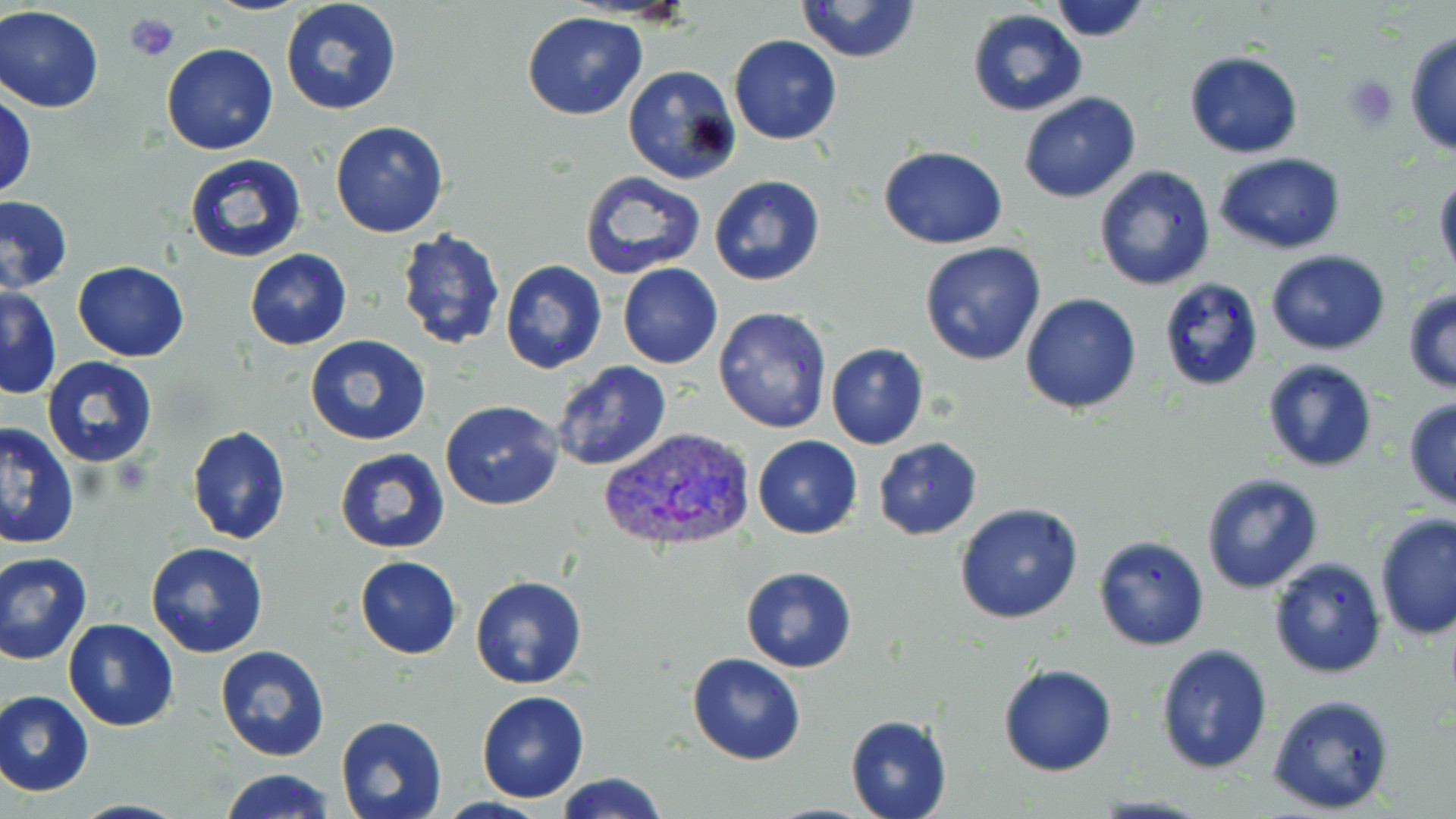
slide-level diagnosis = Plasmodium vivax
modality = light microscopy
magnification = 1000x
platelet locations = approximate bounding boxes as named x1/y1/x2/y2 corners in pixels: (x1=124, y1=11, x2=179, y2=65), (x1=1343, y1=76, x2=1398, y2=130)
uninfected red blood cell locations = approximate bounding boxes as named x1/y1/x2/y2 corners in pixels: (x1=281, y1=0, x2=402, y2=115), (x1=795, y1=0, x2=922, y2=63), (x1=1047, y1=0, x2=1152, y2=42), (x1=0, y1=6, x2=103, y2=114), (x1=967, y1=9, x2=1087, y2=116), (x1=521, y1=11, x2=647, y2=121), (x1=1404, y1=28, x2=1456, y2=160), (x1=729, y1=35, x2=842, y2=145), (x1=161, y1=42, x2=278, y2=155), (x1=1184, y1=52, x2=1303, y2=158), (x1=622, y1=65, x2=741, y2=185), (x1=1017, y1=91, x2=1142, y2=204), (x1=1, y1=93, x2=38, y2=198), (x1=329, y1=120, x2=448, y2=239), (x1=879, y1=145, x2=1007, y2=248), (x1=184, y1=153, x2=308, y2=263), (x1=1215, y1=153, x2=1348, y2=254), (x1=1094, y1=164, x2=1217, y2=293), (x1=579, y1=171, x2=707, y2=279), (x1=1434, y1=172, x2=1456, y2=286), (x1=708, y1=174, x2=826, y2=287), (x1=0, y1=195, x2=72, y2=294), (x1=395, y1=230, x2=505, y2=352), (x1=918, y1=241, x2=1047, y2=366), (x1=244, y1=249, x2=352, y2=349), (x1=1266, y1=249, x2=1390, y2=355), (x1=500, y1=260, x2=607, y2=373), (x1=72, y1=261, x2=190, y2=361), (x1=617, y1=263, x2=723, y2=370), (x1=1160, y1=277, x2=1264, y2=391), (x1=1, y1=286, x2=62, y2=399), (x1=1402, y1=288, x2=1456, y2=395), (x1=1021, y1=293, x2=1142, y2=413), (x1=714, y1=307, x2=833, y2=431), (x1=305, y1=334, x2=432, y2=446), (x1=825, y1=343, x2=929, y2=449), (x1=41, y1=358, x2=160, y2=469), (x1=1260, y1=358, x2=1380, y2=474), (x1=551, y1=361, x2=673, y2=472), (x1=1403, y1=397, x2=1456, y2=512), (x1=440, y1=400, x2=564, y2=511), (x1=0, y1=424, x2=78, y2=550), (x1=187, y1=426, x2=291, y2=545), (x1=751, y1=435, x2=862, y2=540), (x1=873, y1=437, x2=982, y2=540), (x1=334, y1=448, x2=450, y2=553), (x1=1199, y1=472, x2=1323, y2=594), (x1=954, y1=502, x2=1084, y2=625), (x1=1373, y1=513, x2=1456, y2=644), (x1=1093, y1=534, x2=1209, y2=650), (x1=145, y1=542, x2=269, y2=659), (x1=0, y1=551, x2=94, y2=665), (x1=354, y1=556, x2=461, y2=659), (x1=1267, y1=557, x2=1388, y2=678), (x1=740, y1=567, x2=857, y2=672), (x1=471, y1=575, x2=587, y2=688), (x1=63, y1=617, x2=179, y2=731), (x1=1155, y1=643, x2=1273, y2=775), (x1=215, y1=645, x2=330, y2=761), (x1=686, y1=652, x2=808, y2=765), (x1=997, y1=663, x2=1117, y2=776), (x1=0, y1=690, x2=95, y2=796), (x1=476, y1=691, x2=590, y2=803), (x1=1267, y1=692, x2=1397, y2=815), (x1=334, y1=715, x2=447, y2=819), (x1=845, y1=715, x2=952, y2=819), (x1=218, y1=767, x2=335, y2=819), (x1=553, y1=773, x2=673, y2=819)
preparation = thin blood film
field of view = one of a larger specimen
image size = 1456×819 pixels
Plasmodium vivax-infected red blood cell locations = approximate bounding boxes as named x1/y1/x2/y2 corners in pixels: (x1=598, y1=425, x2=757, y2=556)
stain = May-Grünwald-Giemsa